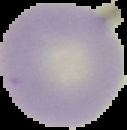
preparation = thin blood smear
image size = 127×130 pixels
result = no Plasmodium parasites detected
image type = cell region segmented out of the field of view; surrounding area masked to black